Assess this cell for malaria.
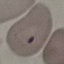
Parasitized.

Giemsa-stained preparation. Photographed with a smartphone camera at the microscope eyepiece. Cell patch, automatically extracted from a larger field of view and resized to 64 × 64 pixels. Thin blood film.